Identify the preparation type.
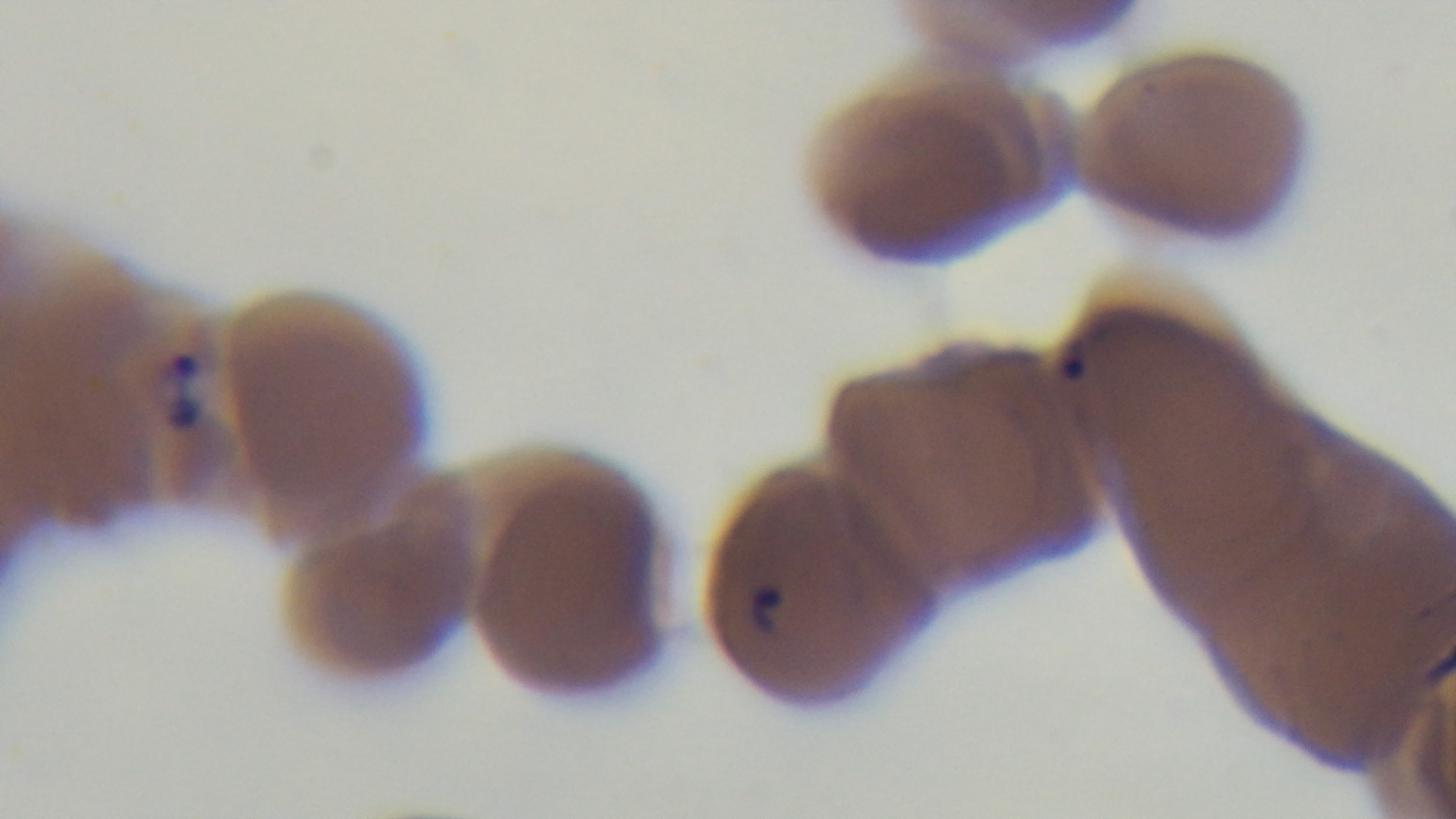

Thin.

Summary:
  - Stain: Giemsa
  - Capture: mounted 4K digital camera
  - Modality: light microscopy
  - Malaria status: positive
  - Objective: 100x oil immersion
  - Field of view: one from the slide